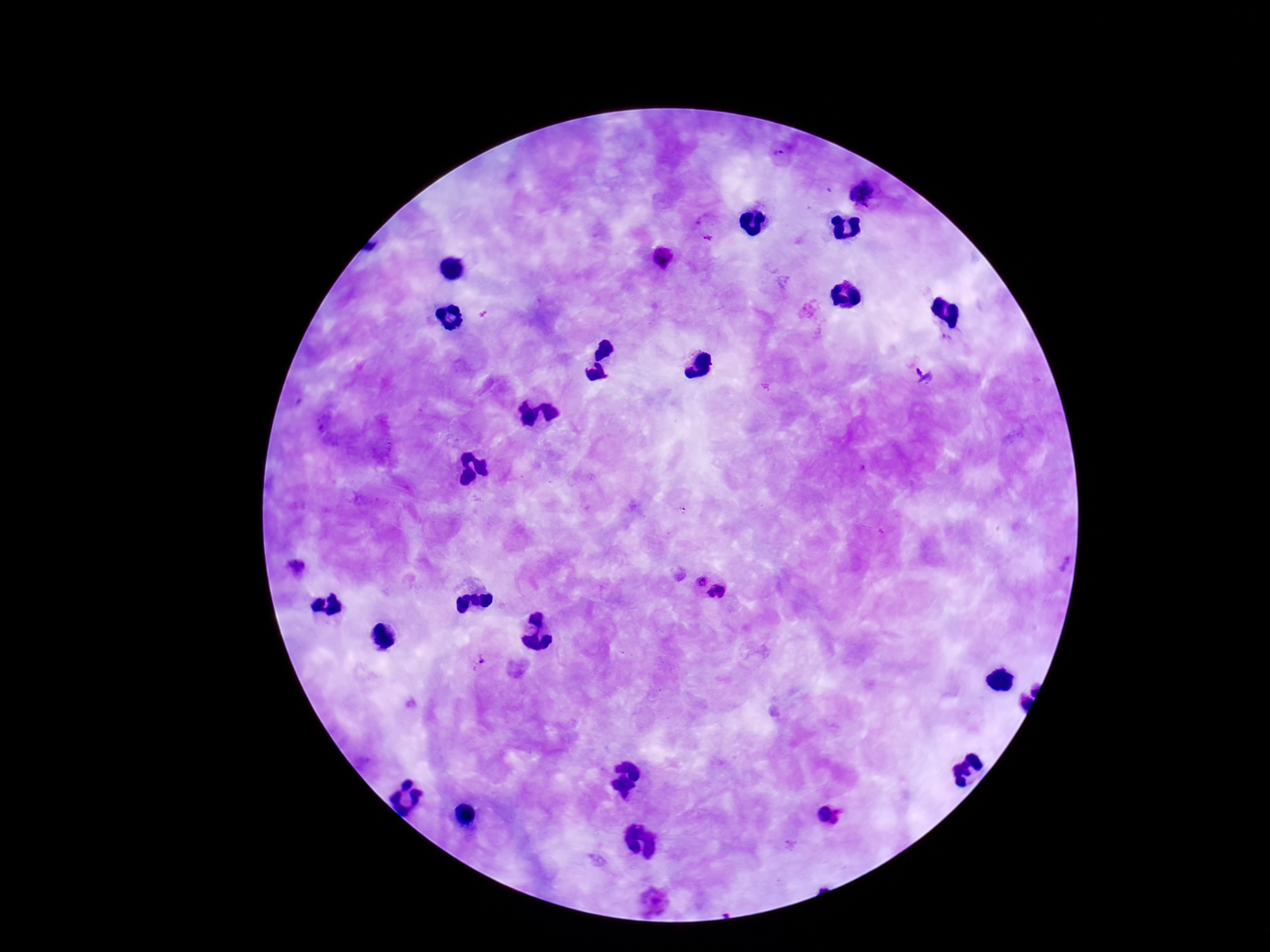
Approximate centers as {x, y} in pixels. Plasmodium parasite locations: {781, 155}, {863, 192}, {664, 258}, {924, 377}, {296, 567}, {701, 579}, {717, 592}, {478, 660}, {831, 816}, {654, 899}. Giemsa stain. One field from this slide. Thick blood smear. Image is 1270×952 pixels. 100x magnification. Photographed through the microscope eyepiece with a smartphone camera. Patient malaria status: infected.